Identify the blood parasite species.
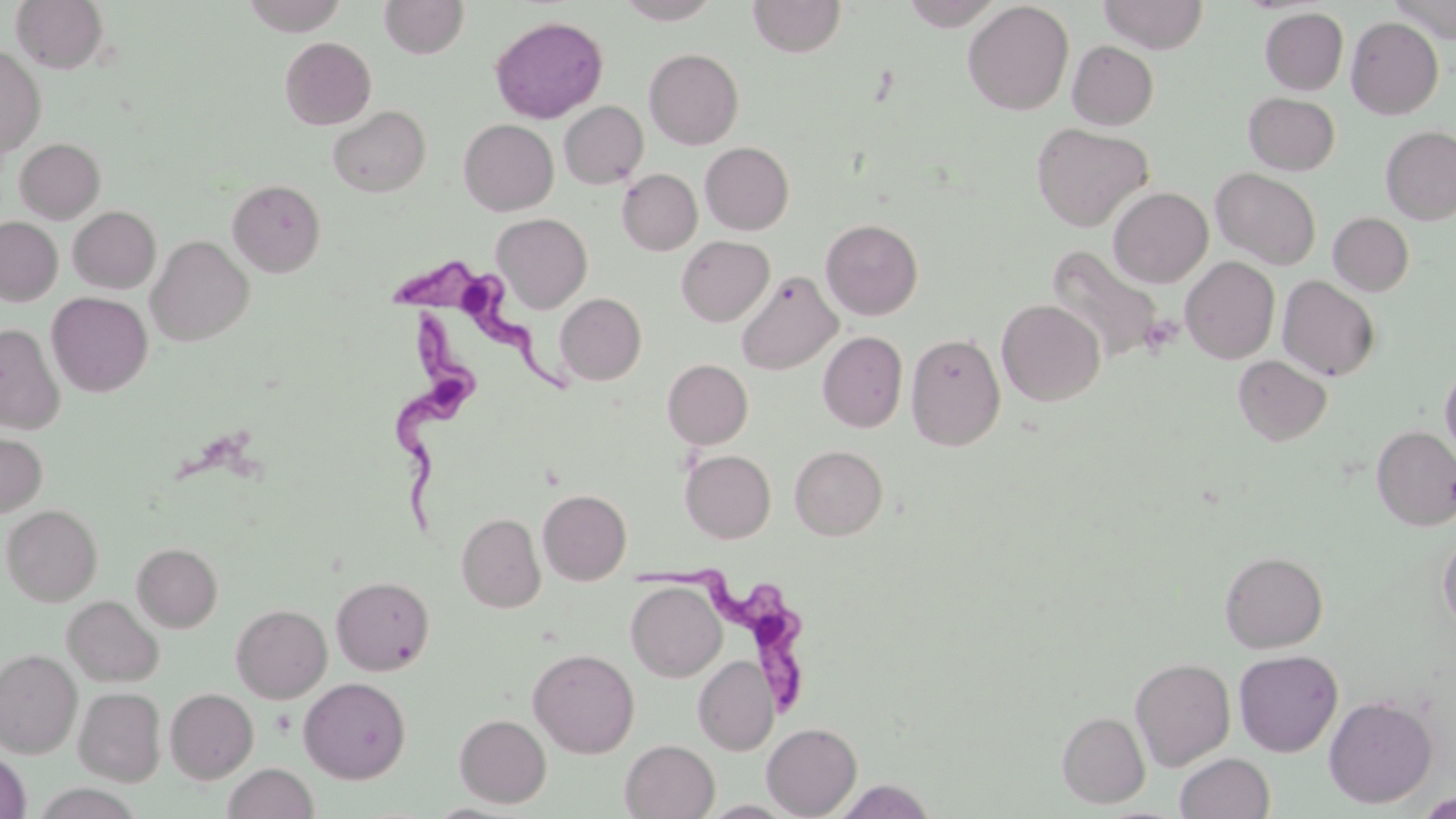
Trypanosoma brucei.

Approximate bounding boxes as (x1, y1, x2, y2) in pixels. Uninfected red blood cell locations: (10, 0, 109, 74), (242, 0, 348, 35), (380, 0, 469, 59), (616, 0, 722, 24), (748, 0, 846, 58), (1097, 0, 1209, 54), (1388, 0, 1456, 43), (899, 1, 1003, 30), (963, 1, 1074, 115), (1260, 8, 1348, 95), (489, 15, 609, 124), (1346, 16, 1443, 119), (280, 36, 376, 130), (1067, 40, 1159, 130), (0, 46, 46, 159), (644, 48, 744, 149), (1243, 92, 1340, 175), (559, 101, 648, 189), (328, 105, 430, 197), (458, 119, 558, 216), (1031, 123, 1153, 232), (1380, 126, 1456, 224), (15, 138, 105, 223), (700, 142, 794, 235), (1211, 168, 1321, 269), (617, 169, 702, 255), (228, 179, 326, 276), (1108, 187, 1213, 288), (68, 206, 160, 293), (1328, 212, 1414, 297), (492, 213, 592, 313), (0, 216, 62, 305), (821, 218, 923, 320), (146, 235, 254, 346), (676, 235, 774, 326), (1045, 244, 1168, 366), (1181, 256, 1279, 364), (737, 270, 842, 374), (1277, 275, 1380, 382), (46, 292, 153, 397), (555, 293, 646, 386), (997, 299, 1105, 406), (0, 322, 65, 434), (818, 331, 908, 433), (906, 333, 1005, 451), (1233, 355, 1332, 445), (662, 359, 753, 449), (1440, 363, 1456, 463), (1371, 425, 1456, 530), (0, 429, 47, 517), (790, 445, 887, 540), (680, 450, 776, 543), (538, 489, 631, 584), (2, 504, 103, 606), (456, 512, 545, 613), (1438, 534, 1456, 634), (132, 543, 222, 632), (1219, 551, 1328, 652), (331, 575, 435, 675), (626, 581, 726, 682), (62, 595, 163, 686), (231, 604, 332, 703), (528, 648, 640, 758), (0, 649, 82, 758), (1233, 649, 1343, 756), (694, 655, 778, 755), (1130, 656, 1236, 770), (299, 677, 411, 783), (74, 687, 165, 786), (165, 688, 258, 783), (1324, 695, 1438, 807), (1057, 711, 1150, 808), (454, 714, 551, 807), (762, 722, 862, 818), (620, 739, 720, 819), (0, 751, 30, 819), (1175, 752, 1274, 819), (223, 763, 318, 819), (831, 779, 937, 819), (1416, 791, 1456, 818), (698, 800, 800, 818). Trypanosoma brucei locations: (393, 261, 568, 392), (378, 310, 484, 533), (631, 556, 816, 713). Platelet locations: (1139, 314, 1182, 357). One field of a larger specimen. May-Grünwald-Giemsa stain. Thin blood smear. Image is 1456×819 pixels. Light microscopy. 1000x magnification.